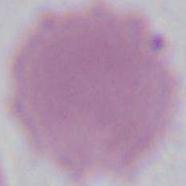 1000x magnification. Photomicrograph. An erythrocyte is seen.